Assess for parasitized red blood cells.
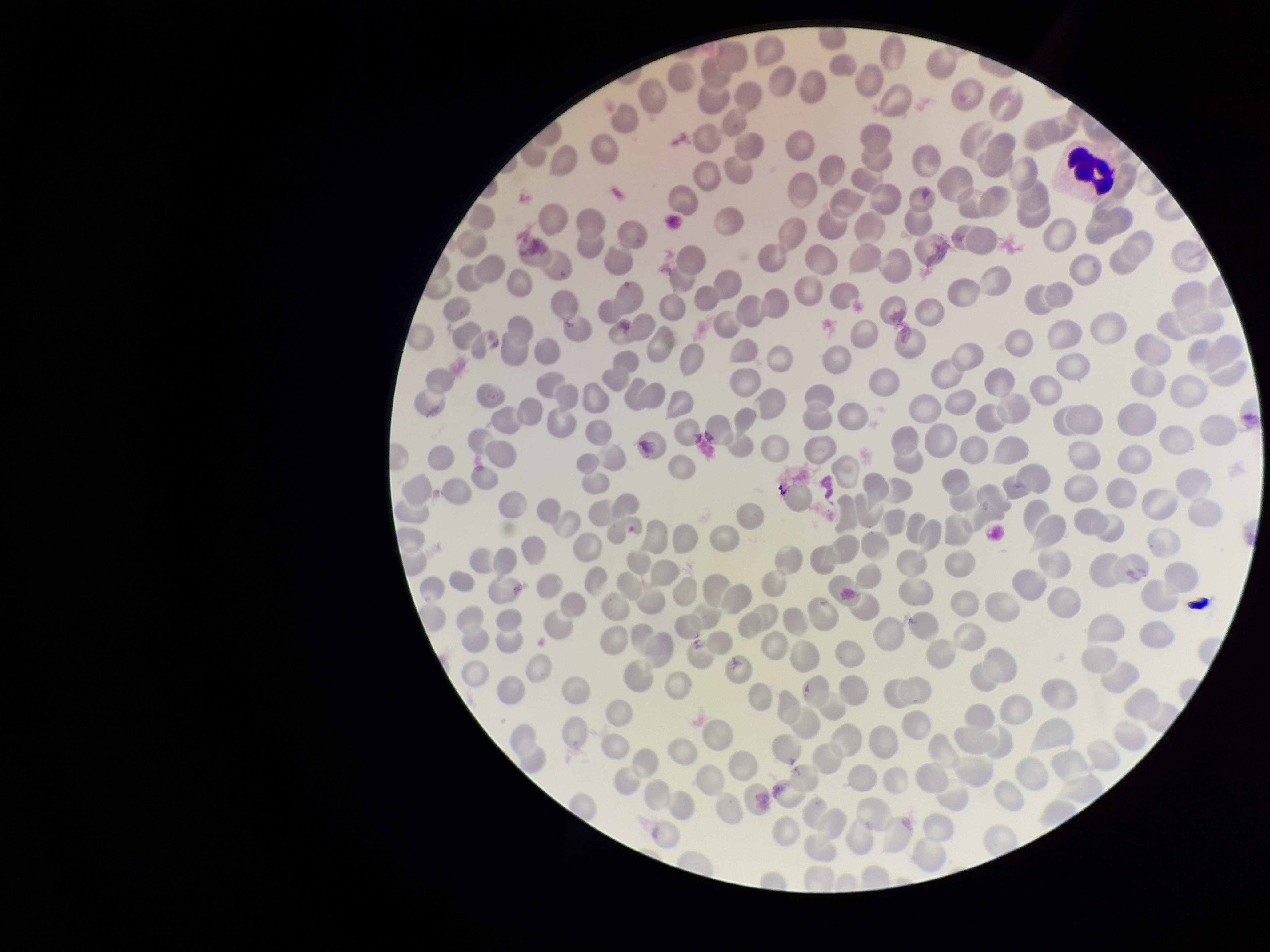

None detected.

image_size: 1270×952 pixels
stain: Giemsa
patient_malaria_status: negative
field_of_view: single
preparation: thin blood smear
capture: smartphone photograph through the microscope eyepiece
red_blood_cell_count: 247
parasitized_red_blood_cell_count: 0